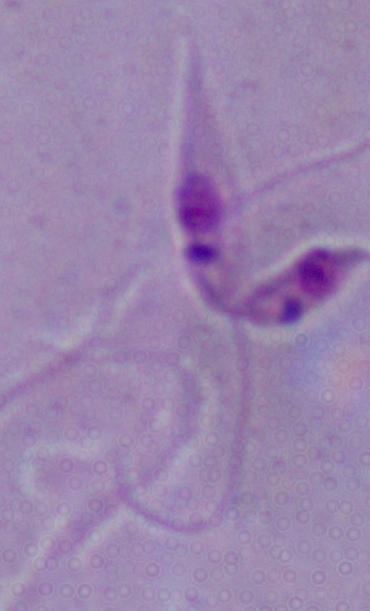
A Leishmania parasite is seen. 1000x magnification. Micrograph.